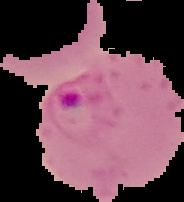

Summary:
  - Image size: 184×202 pixels
  - Result: Plasmodium parasites identified
  - Preparation: thin blood film
  - Image type: segmented cell region with the area outside set to black